Identify the parasite.
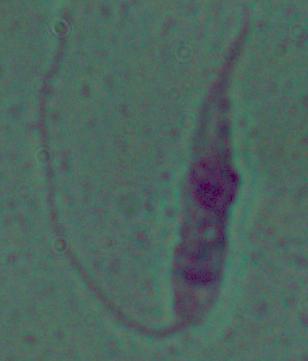

Leishmania.

Summary:
  - Magnification: 1000x
  - Modality: photomicrograph